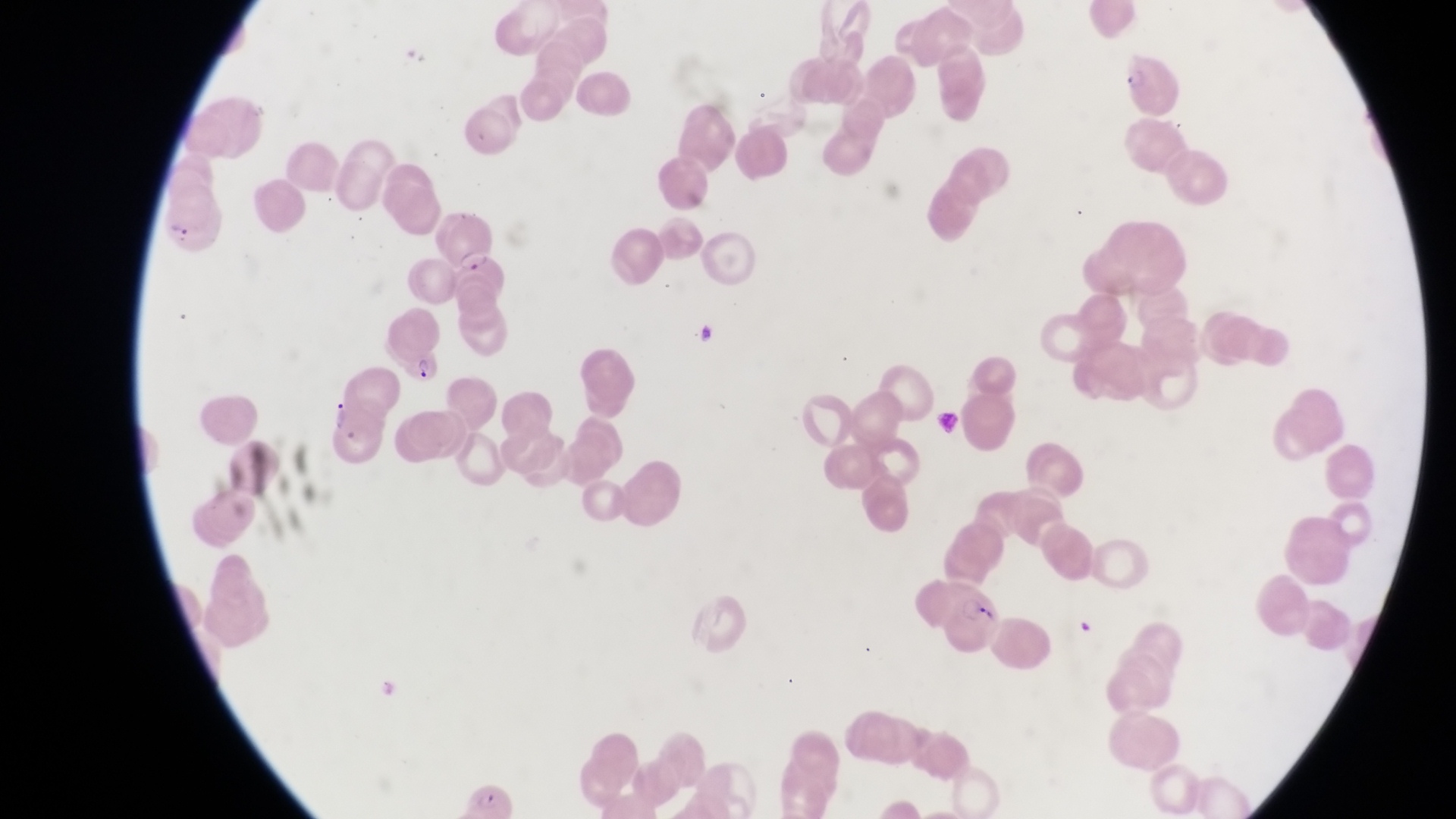

{
  "parasitised_red_blood_cell_locations": "approximate bounding boxes as [left, top, right, bottom] in pixels: [162, 198, 223, 259], [453, 244, 511, 294], [400, 343, 440, 389], [940, 579, 1001, 651]",
  "preparation": "thin blood film",
  "field_of_view": "single",
  "image_size": "1456×819 pixels",
  "magnification": "1000x",
  "capture": "smartphone photograph through the eyepiece of an Olympus CX-23 microscope",
  "country": "Uganda"
}